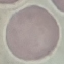 Malaria status: uninfected. Giemsa-stained preparation. Cell patch, automatically extracted from a larger field of view and resized to 64 × 64 pixels. Thin blood film. Photographed with a smartphone camera at the microscope eyepiece.